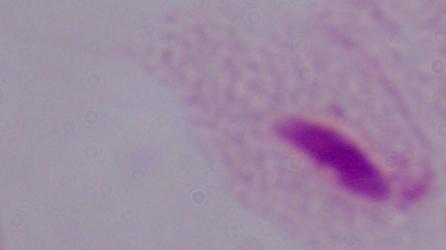

{
  "magnification": "1000x",
  "identification": "trichomonad",
  "modality": "micrograph"
}